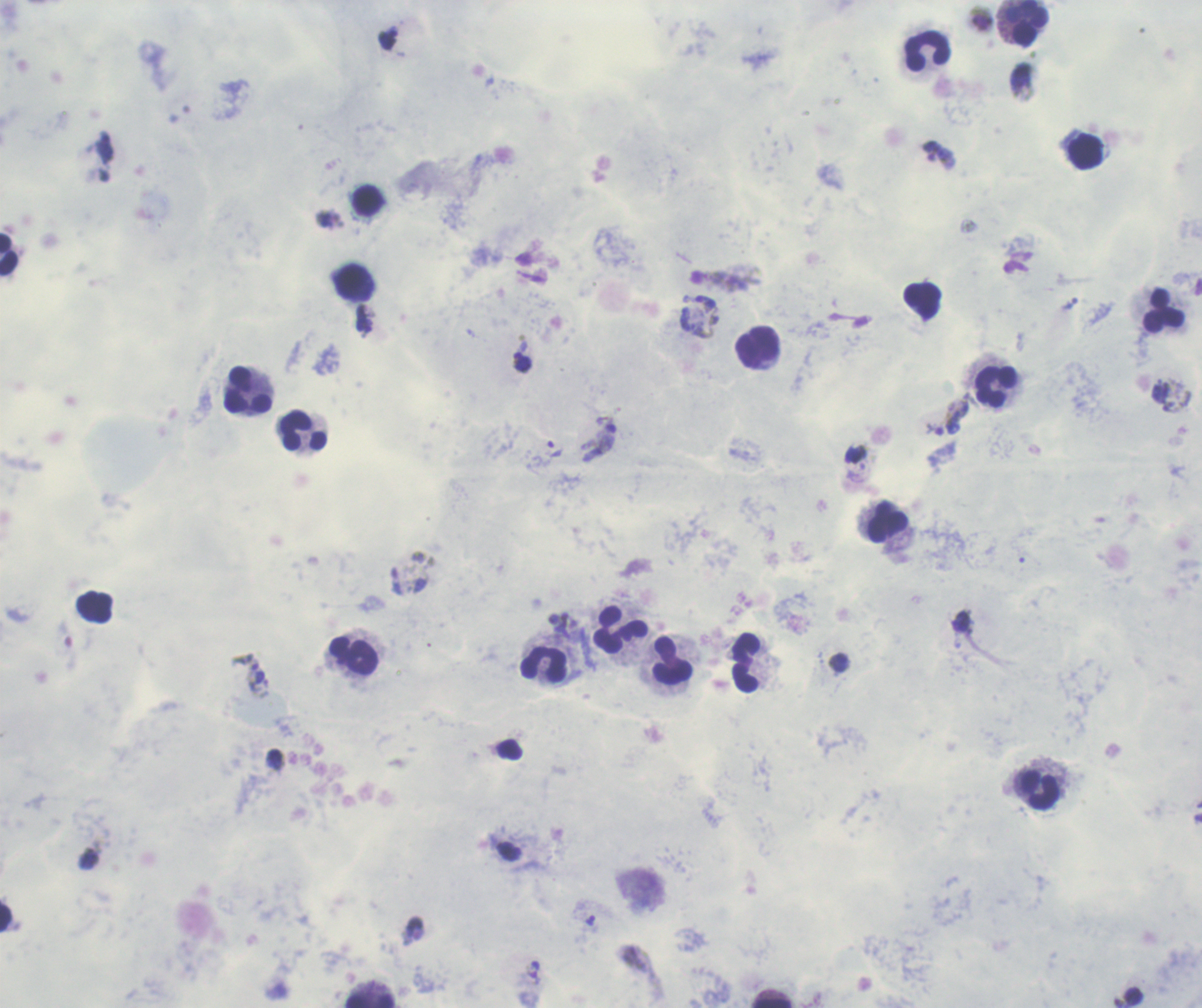

coordinate format = approximate centers as {x, y} in pixels
trophozoite locations = {522, 363}, {952, 418}, {599, 438}, {590, 920}, {413, 931}
gametocyte locations = {717, 280}
leukocyte locations = {1026, 23}, {927, 52}, {1085, 151}, {368, 200}, {10, 256}, {351, 281}, {1164, 310}, {758, 346}, {997, 387}, {248, 391}, {304, 432}, {888, 522}, {620, 631}, {353, 654}, {673, 660}, {746, 662}, {544, 665}, {1039, 791}, {370, 1000}
life-cycle stages observed = trophozoite, gametocyte
image size = 1202×1008 pixels
result = malaria parasites detected
magnification = 100x
preparation = thick smear of blood
background quality = poor
stain = Romanowsky
coloration quality = good
context = previously used in an actual diagnosis
field of view = single